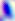 Toxoplasma gondii is seen. Micrograph. 400x magnification.